State which parasite is depicted.
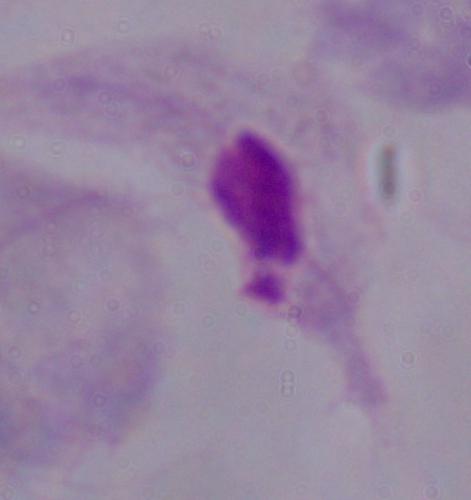
A trichomonad.

Summary:
  - Magnification: 1000x
  - Modality: micrograph